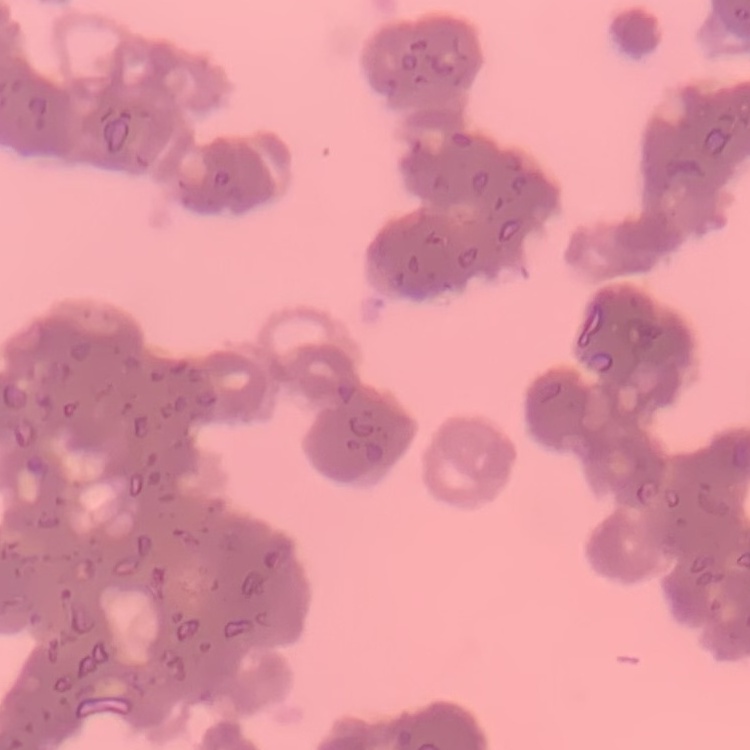
Summary:
  - Erythrocyte morphology: rouleaux formation
  - Image type: one tile cut from a larger photomicrograph
  - Preparation: thin blood film
  - Stain: Field's or Giemsa